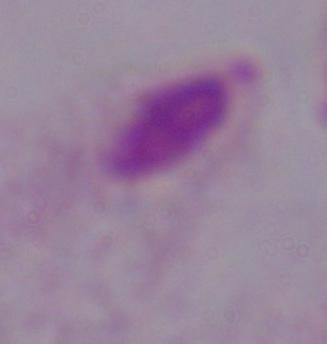

Summary:
  - Magnification: 1000x
  - Modality: photomicrograph
  - Identification: trichomonad